Give the position of every leukocyte visible.
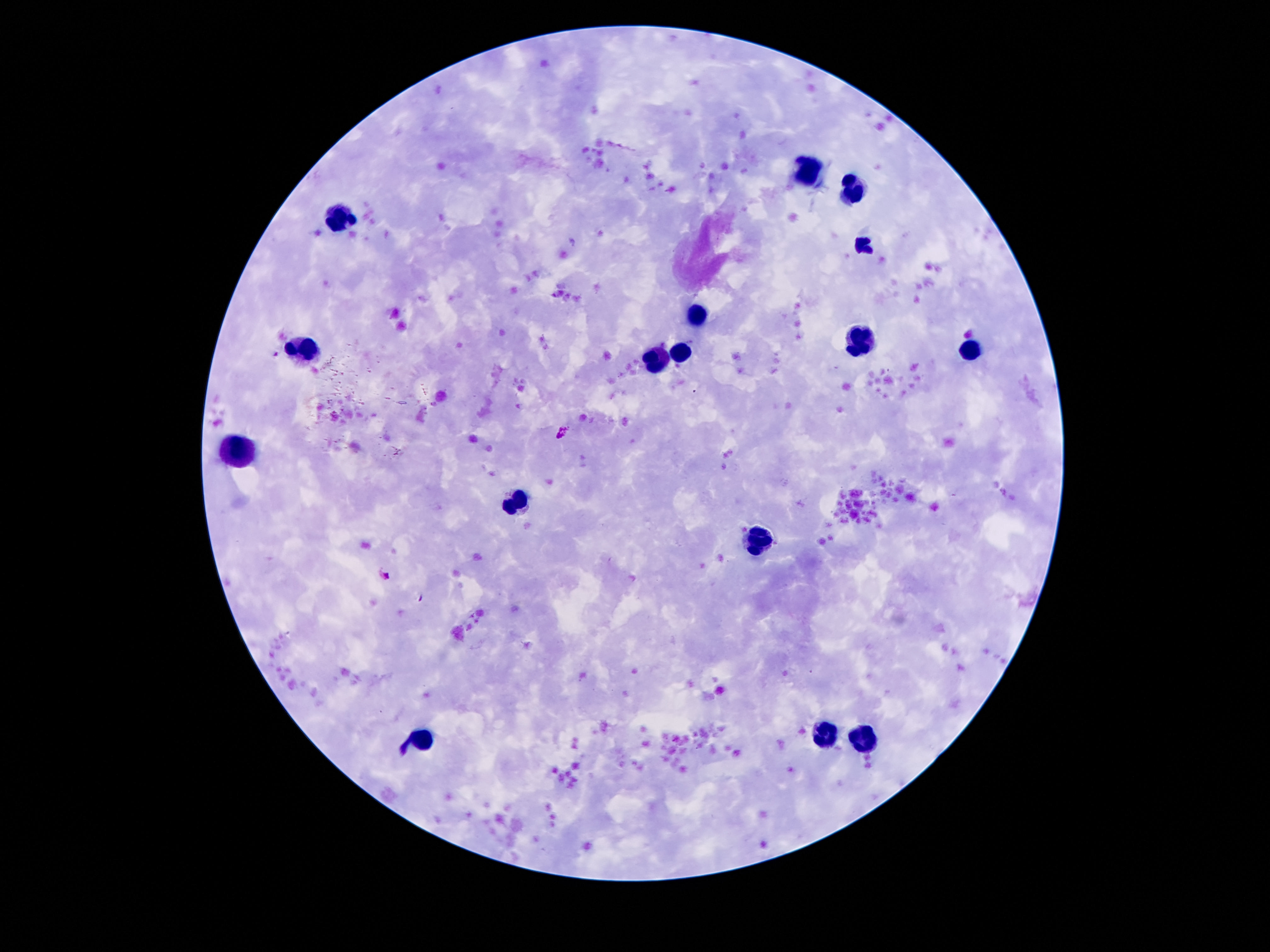

Approximate centers as [x, y] in pixels.
Leukocytes: [807, 167], [853, 185], [344, 215], [695, 317], [861, 338], [303, 345], [970, 348], [680, 350], [657, 360], [239, 452], [517, 500], [759, 541], [825, 732], [863, 737], [423, 740].

patient malaria status = uninfected
stain = Giemsa
preparation = thick peripheral-blood smear
capture = smartphone camera through the microscope eyepiece
magnification = 100x
image size = 1270×952 pixels
field of view = single